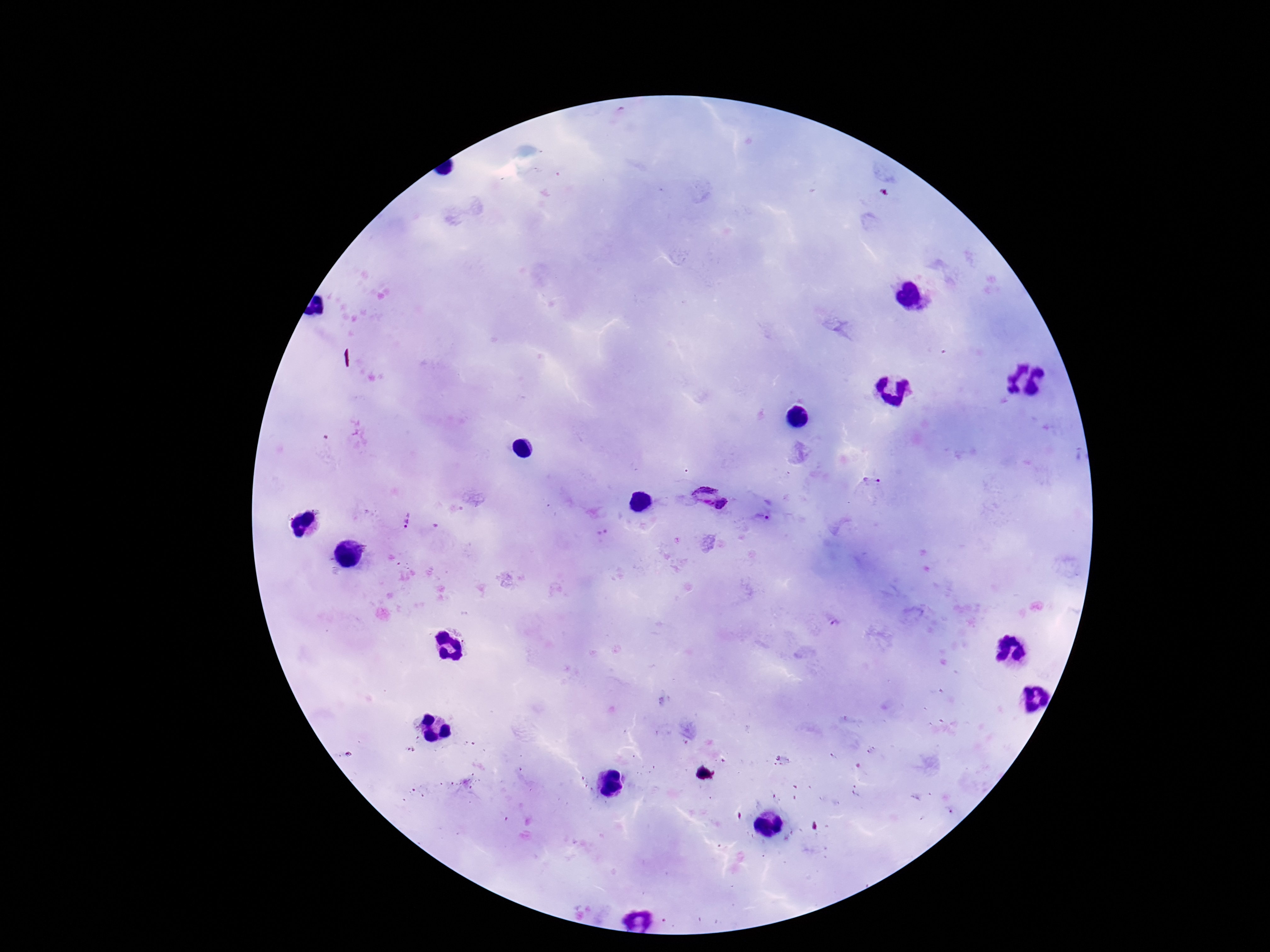

{
  "image_size": "1270×952 pixels",
  "preparation": "thick blood film",
  "plasmodium_parasite_locations": "approximate centers as (x, y) in pixels: (873, 481), (712, 496), (761, 517), (406, 520), (836, 623)",
  "magnification": "100x",
  "capture": "smartphone camera through the microscope eyepiece",
  "field_of_view": "single",
  "stain": "Giemsa",
  "patient_malaria_status": "positive"
}